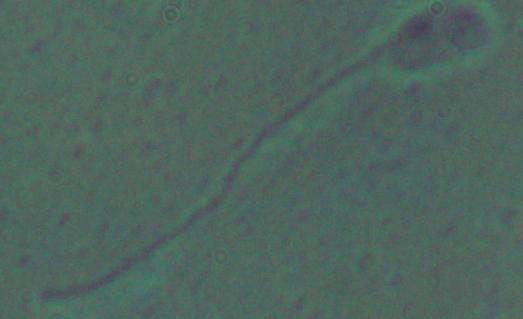
A Leishmania parasite is seen. Photomicrograph. 1000x magnification.